Classify this cell by malaria status.
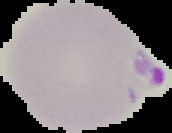
It is parasitized.

image size = 172×133 pixels
preparation = thin blood smear
image type = segmented cell region on a black background